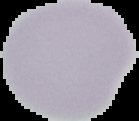
preparation = thin blood smear
image size = 139×121 pixels
image type = cell region segmented out of the field of view; surrounding area masked to black
malaria status = uninfected